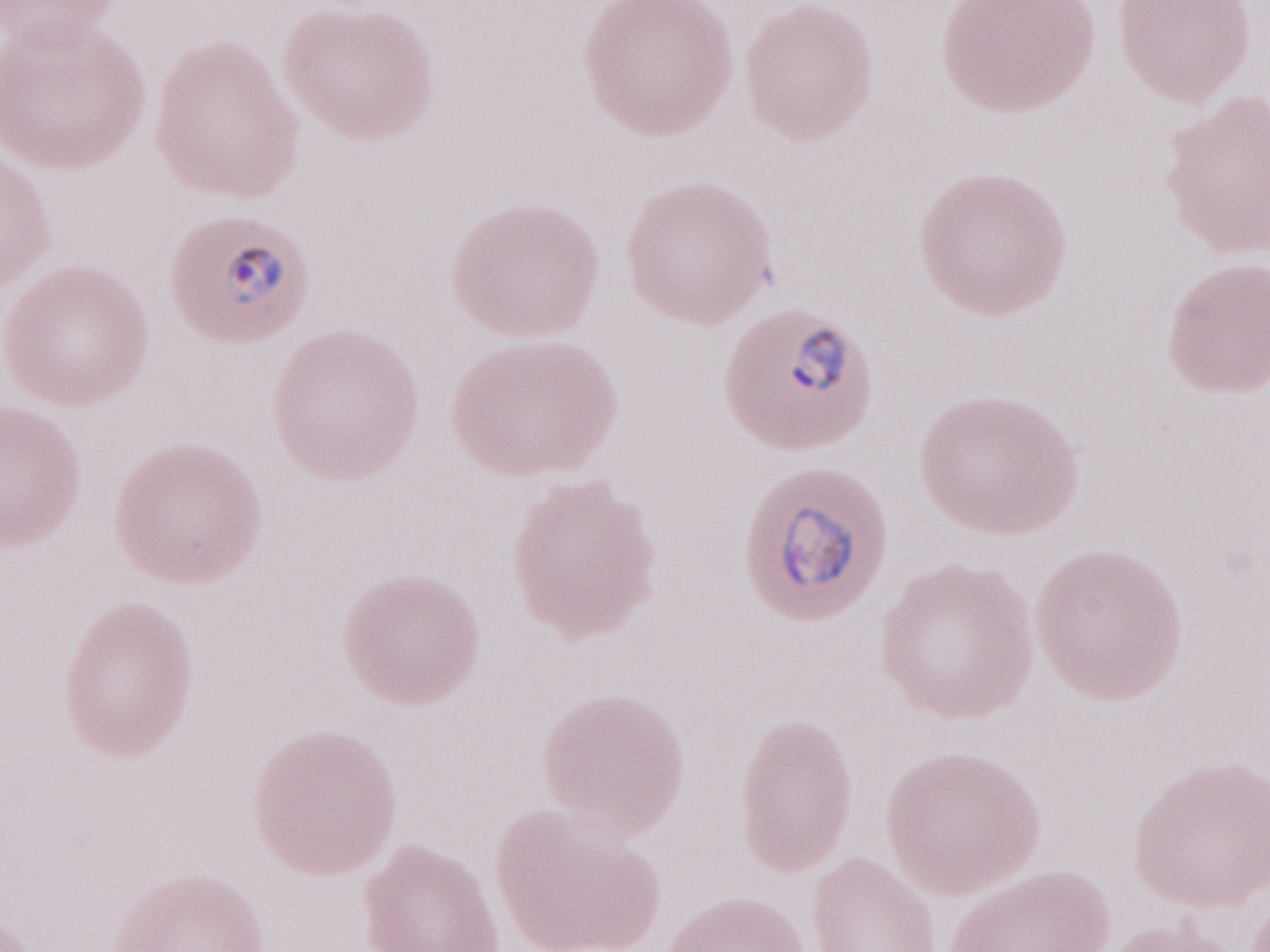 Thin blood film. Patient diagnosis: malaria infection. Image is 1270×952 pixels. May-Grünwald-Giemsa stain. Olympus BX43 microscope, Olympus DP73 camera. One field of this slide. 1,000x magnification.